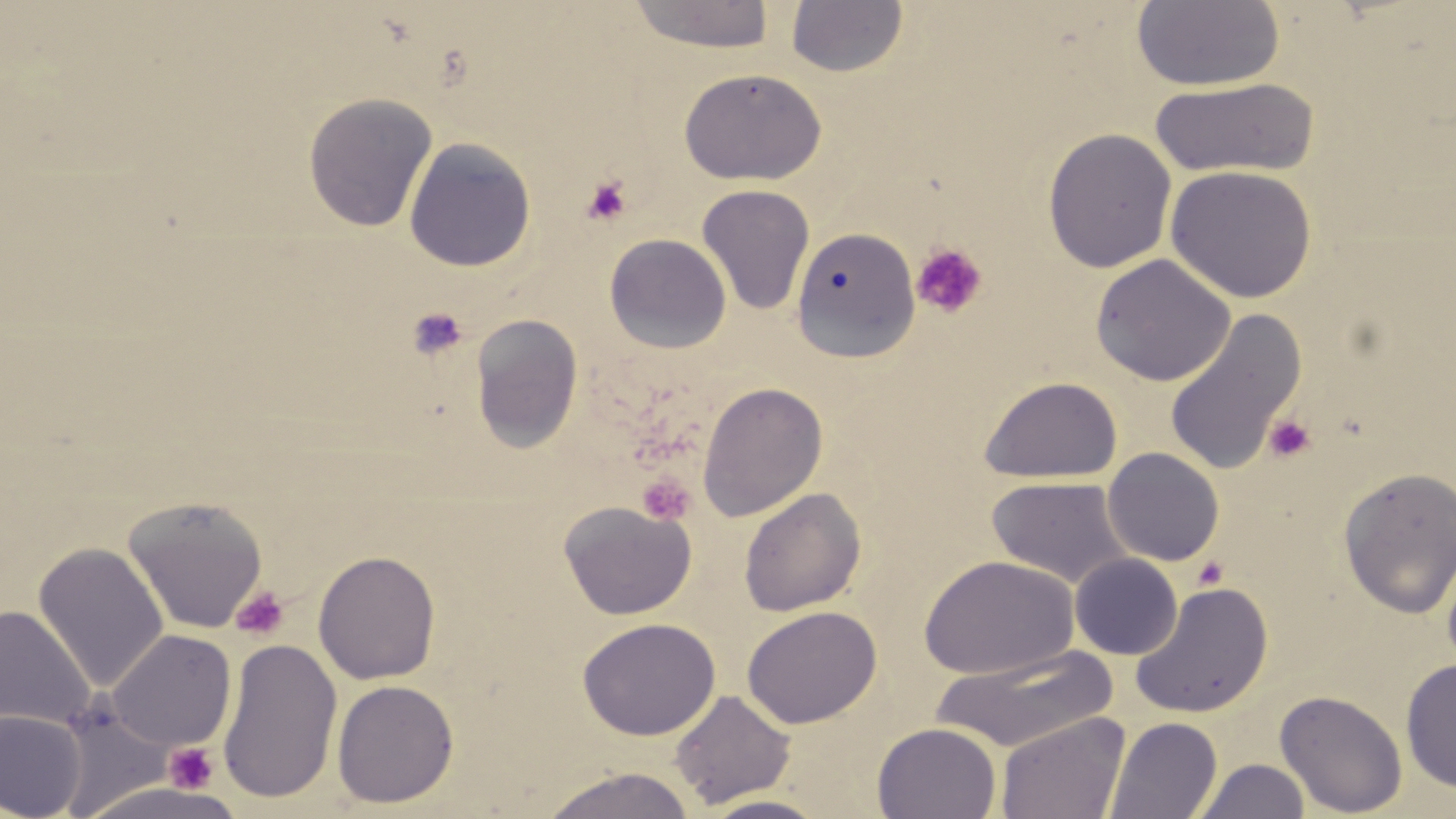

{
  "slide_level_diagnosis": "no evidence of blood parasites",
  "stain": "May-Grünwald-Giemsa",
  "magnification": "1000x",
  "image_size": "1456×819 pixels",
  "preparation": "thin blood film",
  "field_of_view": "single",
  "modality": "light microscopy",
  "uninfected_red_blood_cell_locations": "approximate bounding boxes as named x1/y1/x2/y2 corners in pixels: (x1=624, y1=1, x2=777, y2=53), (x1=785, y1=1, x2=909, y2=78), (x1=1131, y1=1, x2=1286, y2=91), (x1=678, y1=66, x2=827, y2=187), (x1=1148, y1=75, x2=1318, y2=180), (x1=302, y1=91, x2=438, y2=233), (x1=1042, y1=127, x2=1178, y2=273), (x1=403, y1=137, x2=537, y2=272), (x1=1164, y1=165, x2=1318, y2=303), (x1=696, y1=184, x2=815, y2=315), (x1=790, y1=226, x2=921, y2=364), (x1=604, y1=233, x2=732, y2=353), (x1=1090, y1=253, x2=1236, y2=387), (x1=1163, y1=309, x2=1307, y2=477), (x1=469, y1=313, x2=584, y2=453), (x1=978, y1=375, x2=1123, y2=484), (x1=696, y1=381, x2=828, y2=521), (x1=1102, y1=447, x2=1224, y2=566), (x1=1338, y1=467, x2=1456, y2=618), (x1=985, y1=476, x2=1133, y2=589), (x1=738, y1=487, x2=866, y2=618), (x1=122, y1=495, x2=269, y2=634), (x1=558, y1=500, x2=697, y2=621), (x1=33, y1=542, x2=169, y2=692), (x1=312, y1=549, x2=441, y2=684), (x1=919, y1=553, x2=1079, y2=681), (x1=1070, y1=553, x2=1183, y2=659), (x1=1130, y1=581, x2=1274, y2=719), (x1=0, y1=605, x2=96, y2=730), (x1=742, y1=605, x2=881, y2=729), (x1=576, y1=617, x2=721, y2=740), (x1=107, y1=629, x2=237, y2=753), (x1=216, y1=637, x2=343, y2=804), (x1=928, y1=644, x2=1120, y2=753), (x1=1400, y1=657, x2=1456, y2=793), (x1=331, y1=679, x2=459, y2=808), (x1=669, y1=689, x2=796, y2=808), (x1=1275, y1=689, x2=1408, y2=818), (x1=54, y1=693, x2=184, y2=815), (x1=0, y1=710, x2=86, y2=819), (x1=995, y1=711, x2=1130, y2=819), (x1=1104, y1=716, x2=1223, y2=819), (x1=872, y1=722, x2=1001, y2=819), (x1=1193, y1=758, x2=1311, y2=819), (x1=540, y1=767, x2=698, y2=819), (x1=695, y1=794, x2=834, y2=819)",
  "platelet_locations": "approximate bounding boxes as named x1/y1/x2/y2 corners in pixels: (x1=580, y1=175, x2=634, y2=227), (x1=911, y1=243, x2=988, y2=320), (x1=406, y1=307, x2=469, y2=361), (x1=1264, y1=414, x2=1317, y2=463), (x1=636, y1=473, x2=695, y2=525), (x1=1192, y1=556, x2=1229, y2=590), (x1=230, y1=586, x2=291, y2=641), (x1=163, y1=742, x2=219, y2=793)"
}